Point out each Plasmodium parasite and each leukocyte.
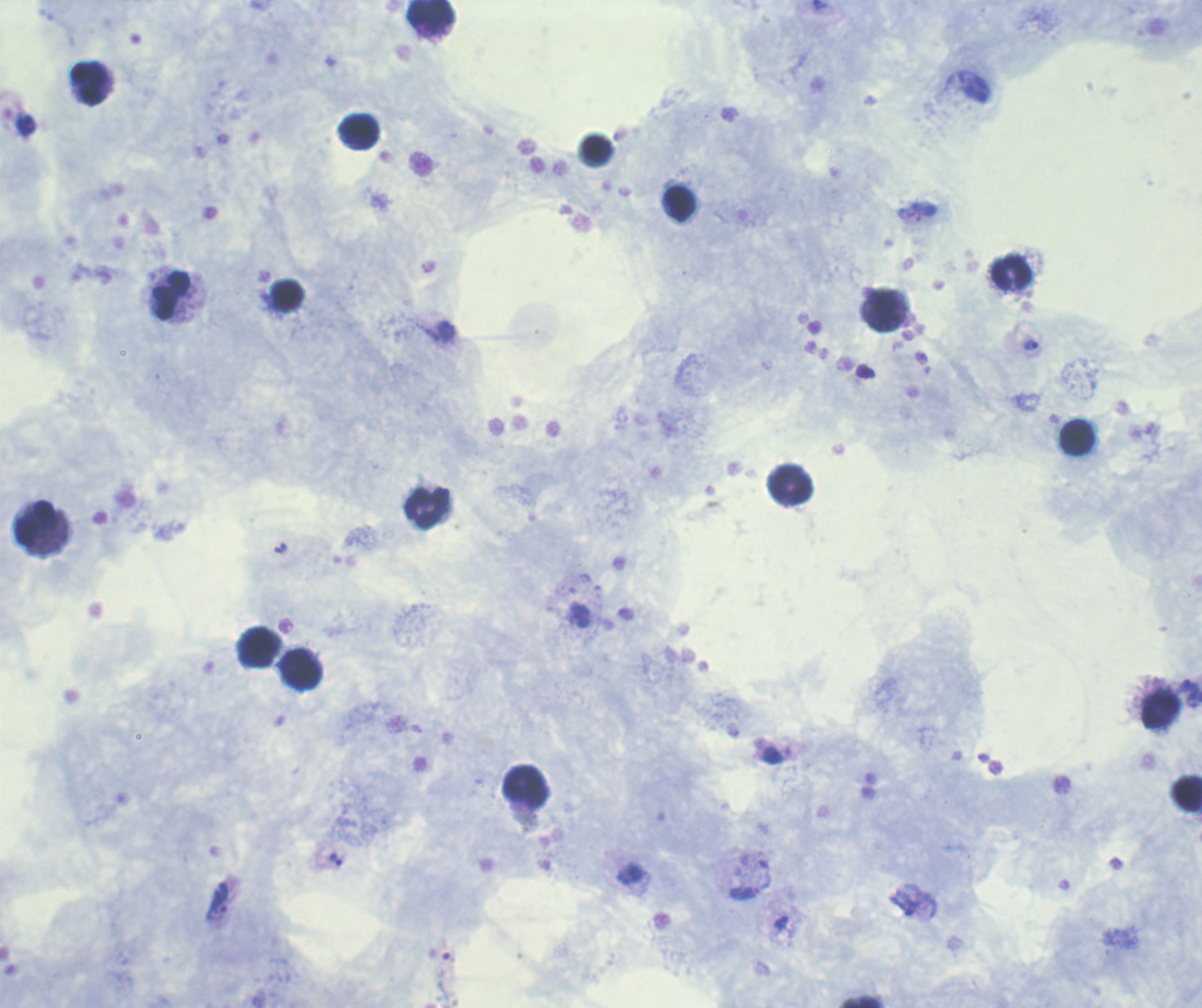

Approximate centers as (x, y) in pixels.
Trophozoites: (447, 331), (1031, 345), (1189, 693), (336, 859), (216, 901), (904, 903), (781, 922).
No schizont or gametocyte forms observed.
Leukocytes: (432, 14), (90, 83), (358, 132), (681, 204), (1012, 274), (172, 295), (286, 295), (882, 309), (1077, 437), (791, 484), (427, 507), (37, 523), (258, 647), (303, 671), (1161, 709), (527, 786).

context: previously used in a real diagnosis
magnification: 100x
field_of_view: single
coloration_quality: good
stain: Romanowsky
background_quality: good
image_size: 1202×1008 pixels
preparation: thick blood smear